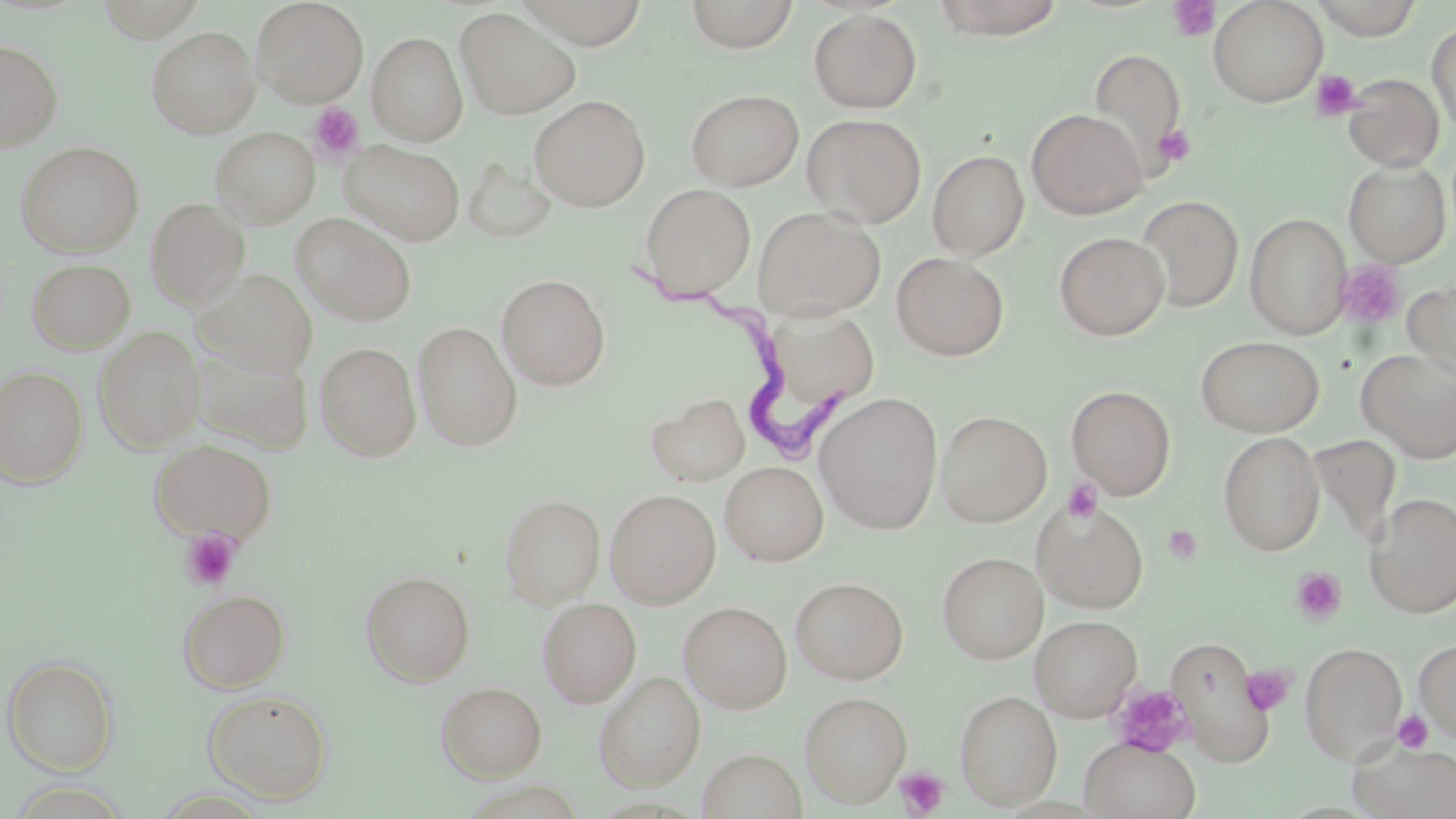

Summary:
  - Coordinate format: approximate bounding boxes as named x1/y1/x2/y2 corners in pixels
  - Uninfected red blood cell locations: (x1=251, y1=0, x2=369, y2=108), (x1=513, y1=0, x2=649, y2=48), (x1=685, y1=0, x2=799, y2=53), (x1=930, y1=0, x2=1066, y2=40), (x1=1208, y1=0, x2=1328, y2=107), (x1=1311, y1=0, x2=1424, y2=40), (x1=94, y1=1, x2=207, y2=42), (x1=456, y1=8, x2=581, y2=120), (x1=809, y1=9, x2=922, y2=113), (x1=1427, y1=22, x2=1456, y2=135), (x1=146, y1=26, x2=261, y2=138), (x1=366, y1=32, x2=467, y2=145), (x1=0, y1=39, x2=63, y2=151), (x1=1087, y1=49, x2=1188, y2=174), (x1=1343, y1=73, x2=1445, y2=172), (x1=685, y1=88, x2=804, y2=192), (x1=529, y1=95, x2=650, y2=212), (x1=1026, y1=108, x2=1147, y2=219), (x1=802, y1=114, x2=927, y2=228), (x1=210, y1=126, x2=320, y2=228), (x1=342, y1=140, x2=465, y2=246), (x1=16, y1=142, x2=144, y2=258), (x1=927, y1=149, x2=1030, y2=261), (x1=462, y1=157, x2=557, y2=244), (x1=1343, y1=161, x2=1450, y2=267), (x1=639, y1=183, x2=756, y2=301), (x1=1138, y1=195, x2=1243, y2=313), (x1=145, y1=199, x2=249, y2=310), (x1=753, y1=206, x2=887, y2=319), (x1=292, y1=213, x2=417, y2=326), (x1=1245, y1=213, x2=1351, y2=339), (x1=1054, y1=231, x2=1169, y2=340), (x1=891, y1=252, x2=1010, y2=361), (x1=27, y1=258, x2=135, y2=354), (x1=195, y1=269, x2=318, y2=377), (x1=496, y1=274, x2=611, y2=391), (x1=1404, y1=278, x2=1456, y2=382), (x1=772, y1=302, x2=886, y2=406), (x1=413, y1=322, x2=523, y2=451), (x1=93, y1=327, x2=204, y2=453), (x1=1195, y1=335, x2=1324, y2=437), (x1=315, y1=341, x2=421, y2=462), (x1=190, y1=346, x2=313, y2=454), (x1=1356, y1=348, x2=1456, y2=462), (x1=1, y1=365, x2=89, y2=489), (x1=1067, y1=385, x2=1176, y2=499), (x1=647, y1=392, x2=750, y2=486), (x1=815, y1=392, x2=944, y2=534), (x1=936, y1=410, x2=1052, y2=527), (x1=1218, y1=431, x2=1325, y2=555), (x1=1307, y1=433, x2=1403, y2=548), (x1=149, y1=439, x2=277, y2=543), (x1=720, y1=461, x2=828, y2=565), (x1=605, y1=489, x2=721, y2=607), (x1=500, y1=494, x2=605, y2=608), (x1=1364, y1=494, x2=1456, y2=617), (x1=1032, y1=496, x2=1149, y2=613), (x1=937, y1=551, x2=1048, y2=664), (x1=360, y1=570, x2=476, y2=686), (x1=790, y1=577, x2=909, y2=684), (x1=177, y1=588, x2=290, y2=693), (x1=537, y1=597, x2=641, y2=708), (x1=679, y1=601, x2=792, y2=713), (x1=1030, y1=615, x2=1142, y2=721), (x1=1164, y1=634, x2=1275, y2=763), (x1=1413, y1=638, x2=1456, y2=744), (x1=1299, y1=642, x2=1407, y2=763), (x1=2, y1=656, x2=118, y2=775), (x1=594, y1=671, x2=705, y2=790), (x1=436, y1=681, x2=547, y2=782), (x1=202, y1=689, x2=333, y2=803), (x1=954, y1=689, x2=1062, y2=809), (x1=800, y1=691, x2=912, y2=807), (x1=1080, y1=737, x2=1201, y2=819), (x1=1350, y1=740, x2=1456, y2=819), (x1=699, y1=748, x2=808, y2=818)
  - Platelet locations: (x1=1168, y1=0, x2=1220, y2=41), (x1=1311, y1=69, x2=1362, y2=121), (x1=308, y1=101, x2=366, y2=162), (x1=1154, y1=124, x2=1196, y2=168), (x1=1335, y1=260, x2=1407, y2=331), (x1=1062, y1=478, x2=1105, y2=525), (x1=1163, y1=525, x2=1203, y2=565), (x1=180, y1=528, x2=241, y2=591), (x1=1290, y1=567, x2=1347, y2=626), (x1=1212, y1=657, x2=1293, y2=731), (x1=1242, y1=665, x2=1295, y2=715), (x1=1109, y1=683, x2=1193, y2=757), (x1=1392, y1=709, x2=1435, y2=753), (x1=894, y1=766, x2=950, y2=817)
  - Trypanosoma brucei locations: (x1=630, y1=263, x2=846, y2=459)
  - Slide-level diagnosis: Trypanosoma brucei
  - Stain: May-Grünwald-Giemsa
  - Image size: 1456×819 pixels
  - Magnification: 1000x
  - Modality: light microscopy
  - Preparation: thin blood film
  - Field of view: one of a larger specimen